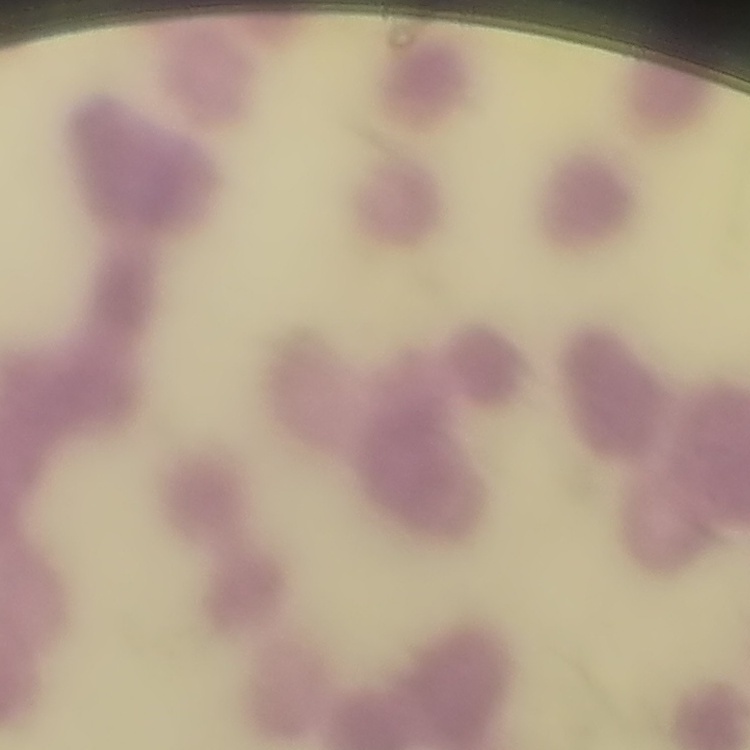

Summary:
  - Erythrocyte morphology: rouleaux formation
  - Stain: Field's or Giemsa
  - Image type: square crop of a larger photomicrograph
  - Preparation: thin blood film